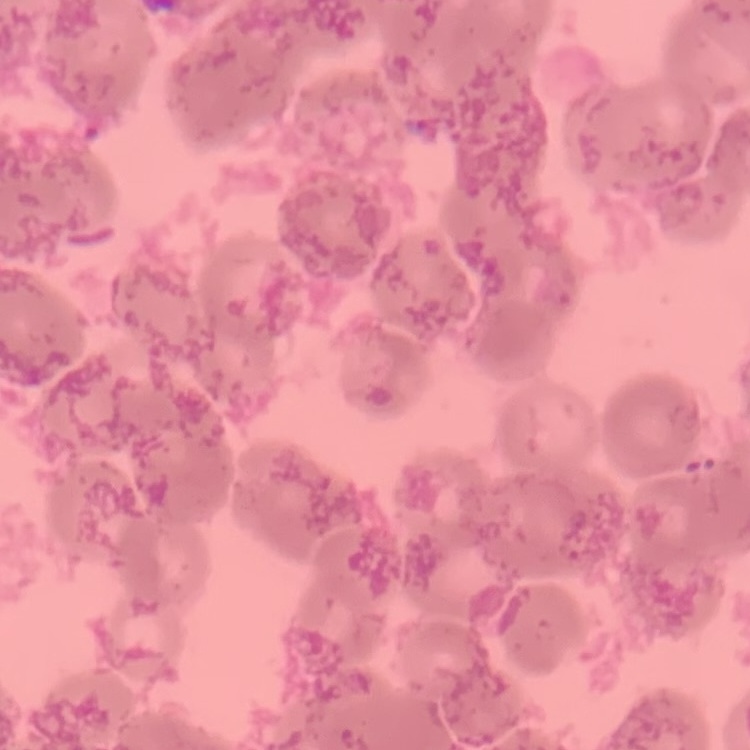
Summary:
  - Red blood cell morphology: rouleaux formation
  - Preparation: thin blood smear
  - Image type: square crop of a larger photomicrograph
  - Stain: Field's or Giemsa